Describe the morphology of the red blood cells.
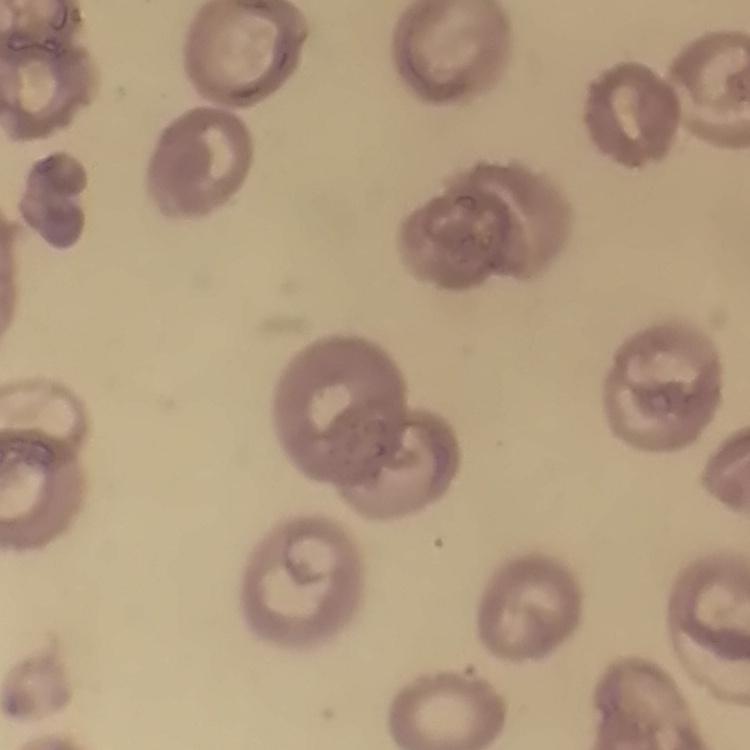

They show no rouleaux formation.

Field's or Giemsa stain. Thin peripheral smear. Square crop of a larger photomicrograph.